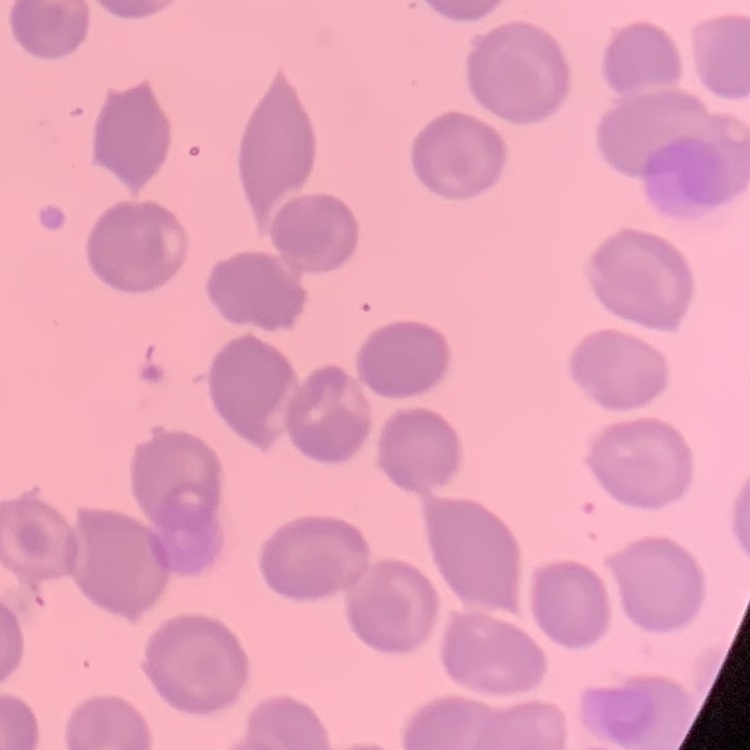
Summary:
  - Erythrocyte morphology: no rouleaux formation
  - Image type: square crop of a larger photomicrograph
  - Preparation: thin blood film
  - Stain: Field's or Giemsa